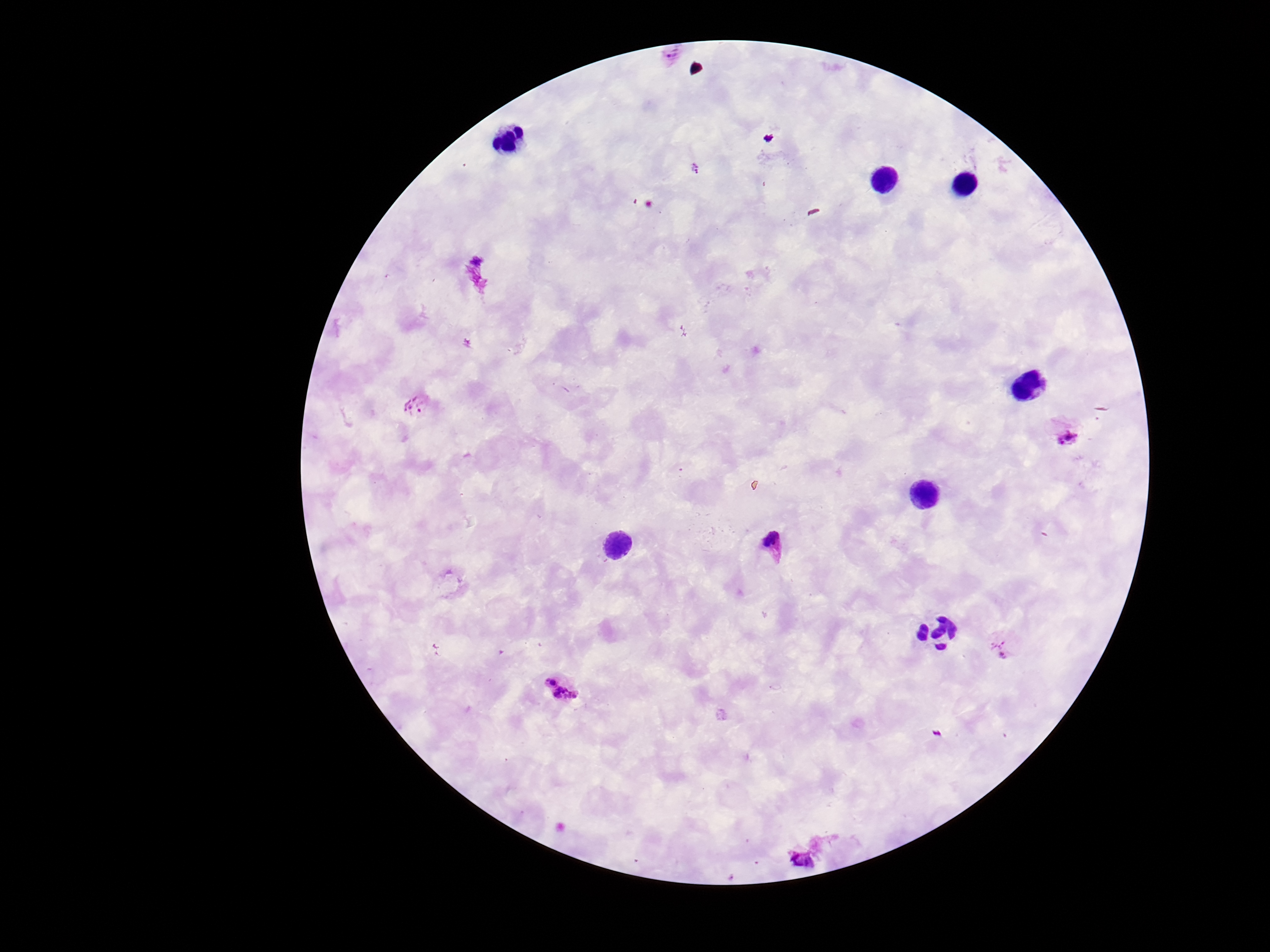
magnification = 100x
capture = smartphone camera through the microscope eyepiece
image size = 1270×952 pixels
patient malaria status = positive
field of view = one from this slide
preparation = thick blood smear
Plasmodium parasite locations = approximate centers as (x, y) in pixels: (416, 406), (1070, 440), (773, 545), (1002, 646), (560, 690), (805, 862)
stain = Giemsa